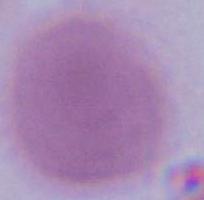
Summary:
  - Magnification: 1000x
  - Modality: micrograph
  - Identification: erythrocyte